Classify this cell by malaria status.
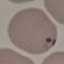
Parasitized.

image type = automatically extracted cell patch, resized to 64 × 64 pixels
stain = Giemsa
preparation = thin blood film
capture = smartphone through the microscope eyepiece